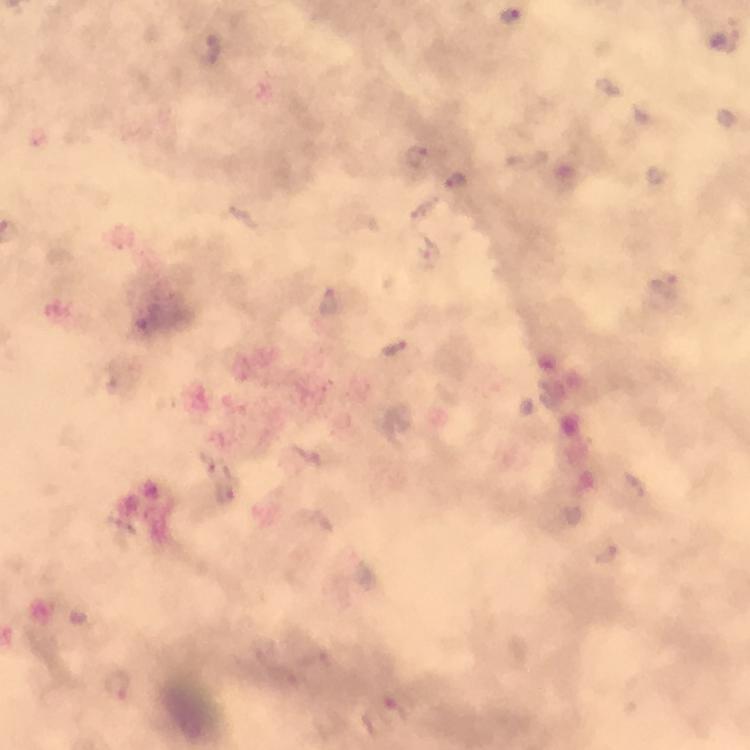

Approximate object centers, in pixels from the top-left corner. Plasmodium parasite locations: (x=513, y=16), (x=723, y=39), (x=204, y=49), (x=417, y=155), (x=456, y=180), (x=664, y=285), (x=328, y=304), (x=396, y=349), (x=117, y=683), (x=394, y=710). Immersion oil applied. 100x magnification. A crop from one field of view. Thick blood film. Image is 750×750 pixels. From a diagnostic examination for malaria. Smartphone photograph taken through a microscope. Giemsa-stained preparation.